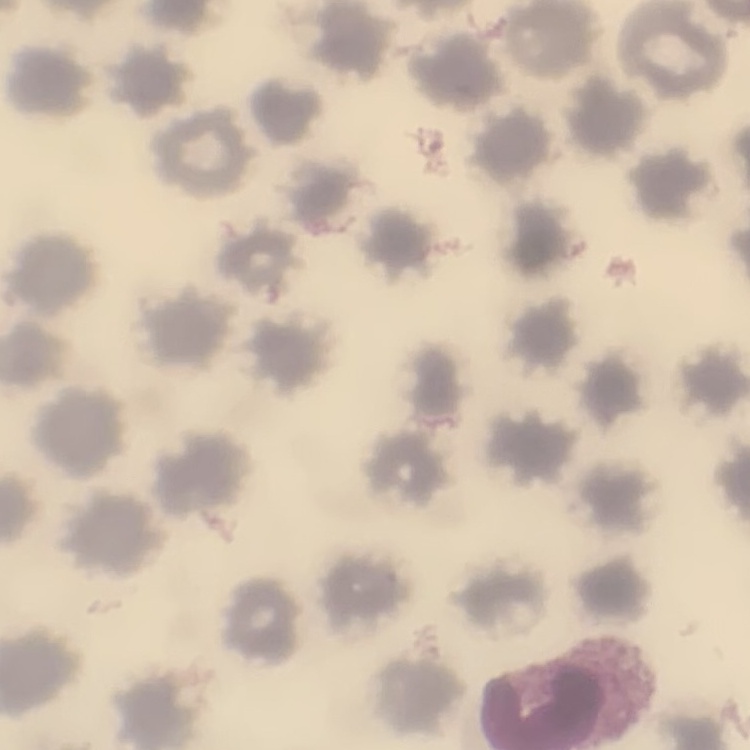
Summary:
  - Red blood cell morphology: no rouleaux formation
  - Stain: Field's or Giemsa
  - Image type: one tile cut from a larger photomicrograph
  - Preparation: thin blood smear